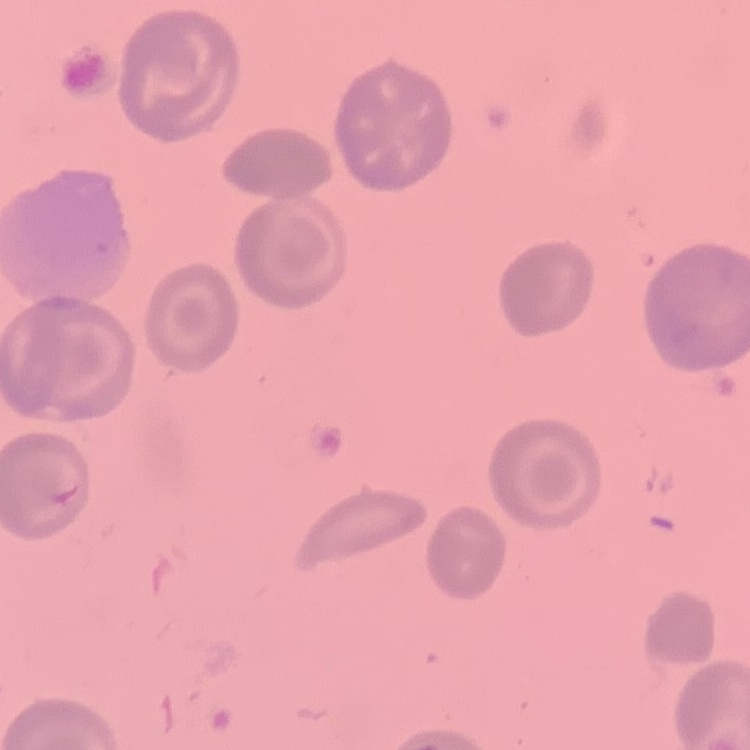

The red blood cells show no rouleaux formation. One tile cut from a larger photomicrograph. Thin blood smear. Stained with either Field's or Giemsa.